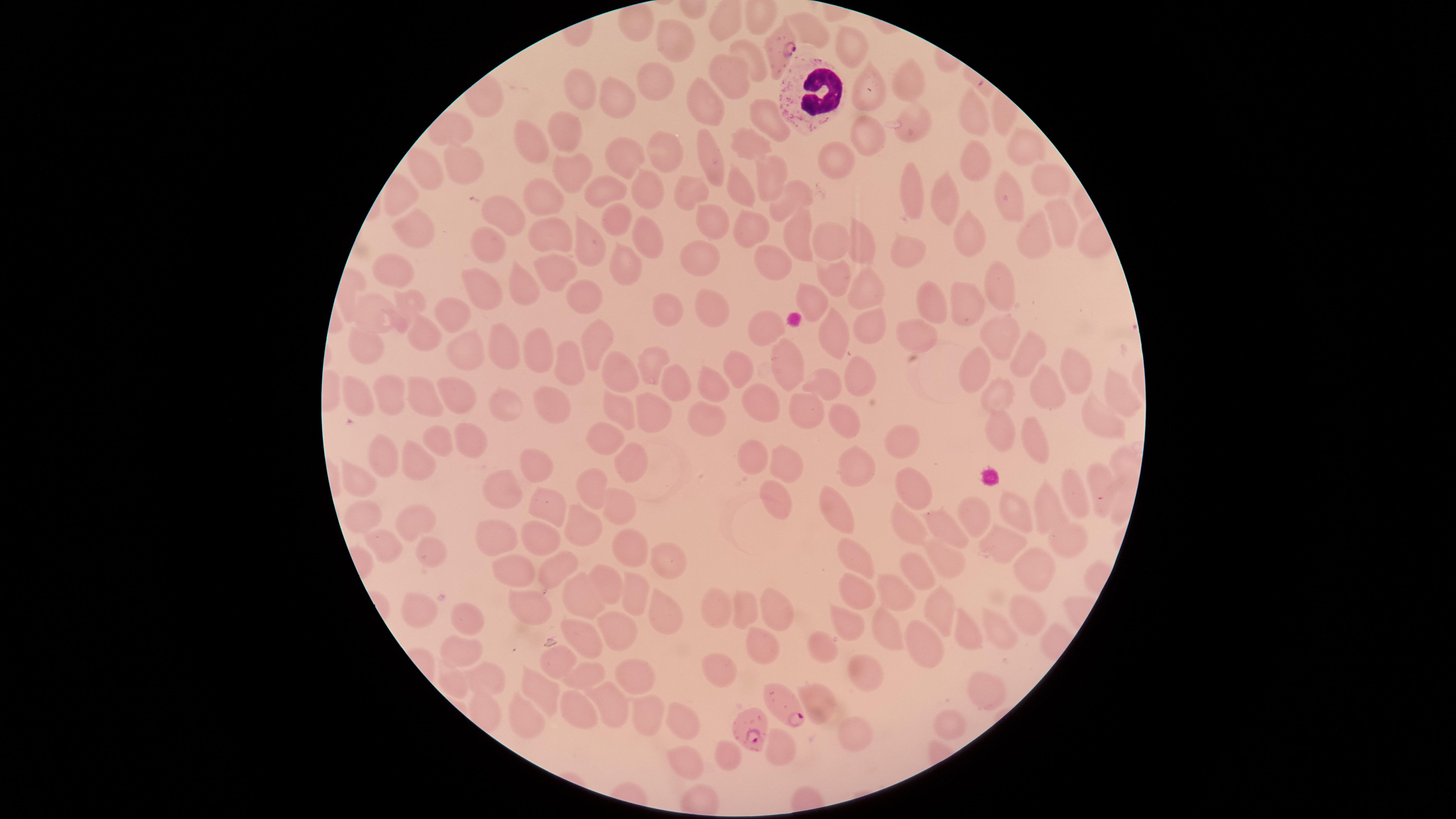
Approximate marker points as (x, y) in pixels. Uninfected RBCs: (813, 31), (683, 39), (849, 46), (752, 56), (730, 69), (656, 76), (909, 82), (867, 90), (581, 94), (617, 99), (710, 102), (765, 117), (974, 120), (910, 125), (568, 130), (868, 135), (751, 137), (529, 140), (1022, 147), (663, 148), (974, 154), (621, 159), (718, 159), (835, 163), (467, 165), (568, 168), (772, 173), (1046, 176), (421, 177), (601, 185), (910, 186), (647, 187), (739, 189), (684, 190), (543, 194), (1012, 195), (797, 196), (946, 206), (1056, 214), (618, 215), (498, 217), (706, 227), (417, 228), (547, 230), (640, 231), (798, 231), (971, 232), (751, 233), (1028, 238), (487, 241), (830, 241), (587, 244), (862, 244), (904, 247), (775, 260), (699, 261), (398, 267), (548, 268), (623, 269), (480, 282), (830, 282), (522, 284), (867, 285), (997, 285), (815, 296), (587, 297), (410, 302), (967, 302), (928, 306), (370, 308), (711, 311), (450, 312), (660, 313), (860, 324), (991, 329), (766, 334), (918, 334), (834, 338), (1022, 343), (363, 344), (593, 344), (471, 347), (535, 350), (502, 351), (571, 359), (650, 362), (736, 364), (1072, 368), (976, 370), (784, 373), (620, 375), (670, 377), (706, 377), (863, 377), (830, 384), (1047, 385), (389, 389), (1114, 391), (354, 392), (455, 393), (417, 394), (998, 396), (548, 400), (766, 401), (621, 404), (506, 406), (799, 410), (651, 414), (847, 414), (1098, 414), (704, 415), (998, 429), (606, 433), (466, 438), (436, 440), (905, 441), (1040, 444), (385, 456), (751, 457), (785, 459), (413, 460), (633, 462), (857, 468), (534, 471), (914, 477), (360, 482), (593, 485), (1098, 485), (500, 490), (1079, 493), (544, 498), (775, 498), (619, 499), (1047, 507), (361, 508), (835, 510), (1019, 511), (973, 514), (418, 523), (581, 527), (906, 527), (949, 528), (539, 534), (1061, 538), (494, 540), (1000, 540), (628, 547), (389, 551), (943, 552), (855, 553), (427, 557), (664, 563), (552, 568), (510, 570), (1030, 570), (913, 571), (610, 586), (855, 586), (897, 590), (586, 593), (635, 595), (419, 606), (529, 606), (745, 607), (936, 607), (1022, 611), (662, 612), (717, 612), (467, 618), (768, 618), (847, 621), (622, 627), (998, 631), (964, 632), (889, 633), (581, 639), (756, 645), (826, 645), (922, 646), (460, 652), (560, 660), (582, 667), (725, 671), (867, 674), (632, 675), (484, 678), (451, 685), (542, 692), (820, 693), (981, 695), (610, 706), (575, 714), (645, 717), (522, 721), (687, 721), (856, 729), (725, 756), (692, 763). WBCs: (806, 90). Parasitized RBCs: (778, 42), (792, 706), (750, 724). Photographed with a smartphone camera through the microscope eyepiece. Giemsa stain. Circular visible region. Species: Plasmodium falciparum. Thin smear of blood. Presence: malaria parasites seen. Image is 1456×819 pixels. One field of view of the specimen.